Classify this cell by malaria status.
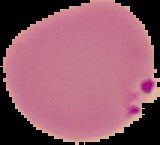
Parasitized.

Image is 160×145 pixels. The area outside the segmented cell region is set to black. From a thin blood smear.